Locate every blood parasite and identify its species.
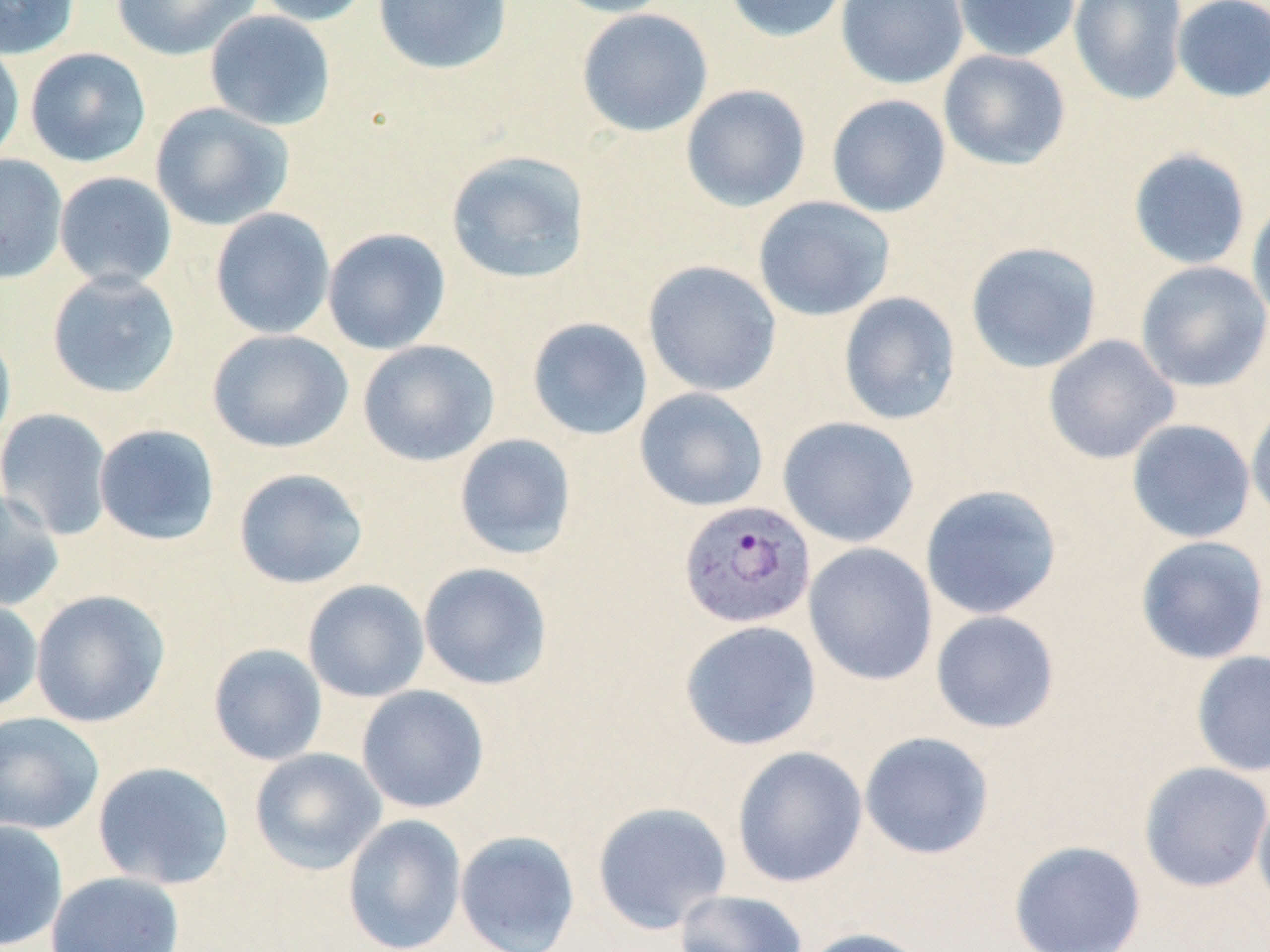
Approximate bounding boxes as (x1, y1, x2, y2) in pixels.
Plasmodium vivax-infected red blood cells: (678, 500, 817, 630).
No Plasmodium falciparum, Plasmodium ovale, Plasmodium malariae, Babesia divergens, or Trypanosoma brucei observed.

Uninfected red blood cell locations: (0, 0, 80, 60), (110, 0, 262, 61), (251, 0, 375, 26), (373, 0, 513, 75), (546, 0, 679, 18), (723, 0, 853, 43), (836, 0, 969, 89), (953, 0, 1080, 62), (1068, 0, 1189, 105), (1171, 0, 1270, 103), (576, 8, 714, 137), (204, 10, 336, 131), (0, 40, 25, 165), (25, 48, 151, 167), (938, 49, 1071, 171), (680, 84, 811, 212), (826, 94, 952, 218), (150, 102, 295, 231), (1127, 148, 1252, 271), (445, 150, 591, 285), (0, 153, 68, 284), (54, 171, 178, 289), (1247, 194, 1270, 328), (753, 196, 896, 321), (209, 207, 336, 340), (322, 227, 451, 355), (965, 241, 1103, 373), (642, 260, 782, 396), (1135, 261, 1270, 392), (46, 270, 181, 398), (837, 292, 961, 426), (527, 317, 653, 441), (0, 325, 16, 452), (207, 329, 354, 453), (1043, 335, 1180, 465), (357, 339, 500, 467), (634, 387, 769, 512), (1246, 397, 1270, 526), (0, 408, 114, 540), (777, 416, 920, 547), (1126, 418, 1256, 544), (93, 424, 221, 545), (454, 433, 577, 560), (233, 467, 369, 589), (920, 484, 1063, 620), (0, 488, 65, 612), (1135, 535, 1270, 664), (803, 542, 938, 686), (418, 562, 553, 690), (303, 579, 430, 703), (30, 589, 170, 728), (0, 597, 43, 713), (930, 610, 1060, 734), (679, 620, 822, 751), (208, 643, 328, 766), (1190, 650, 1270, 778), (356, 685, 489, 814), (0, 711, 105, 835), (859, 731, 995, 860), (731, 745, 868, 888), (249, 748, 387, 875), (92, 761, 235, 890), (1138, 761, 1270, 893), (1252, 789, 1270, 914), (592, 801, 733, 934), (342, 814, 467, 952), (0, 820, 69, 951), (455, 830, 581, 952), (1008, 840, 1147, 952), (46, 871, 185, 952), (673, 889, 808, 952), (796, 927, 931, 952). Slide-level diagnosis: Plasmodium vivax. Light microscopy. May-Grünwald-Giemsa stain. Single field of view. Captured at 1000x magnification. Image is 1270×952 pixels. Thin blood smear.